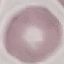

Result: no malaria parasites detected. Cell patch, automatically extracted from a larger field of view and resized to 64 × 64 pixels. Giemsa stain. Acquired by smartphone through the microscope eyepiece. Thin smear of blood.